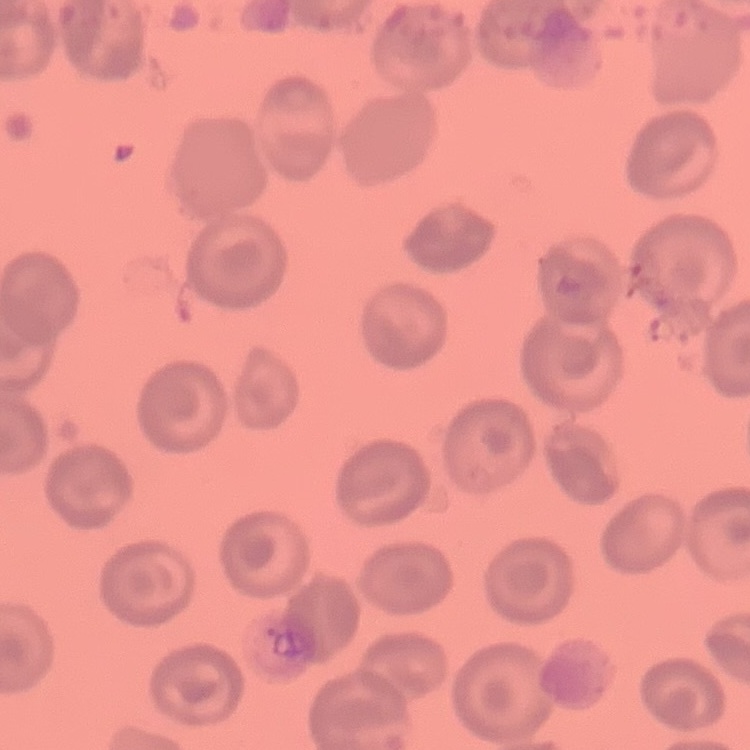

Summary:
  - Erythrocyte morphology: no rouleaux formation
  - Image type: one tile cut from a larger photomicrograph
  - Stain: Field's or Giemsa
  - Preparation: thin peripheral smear